Give the preparation type.
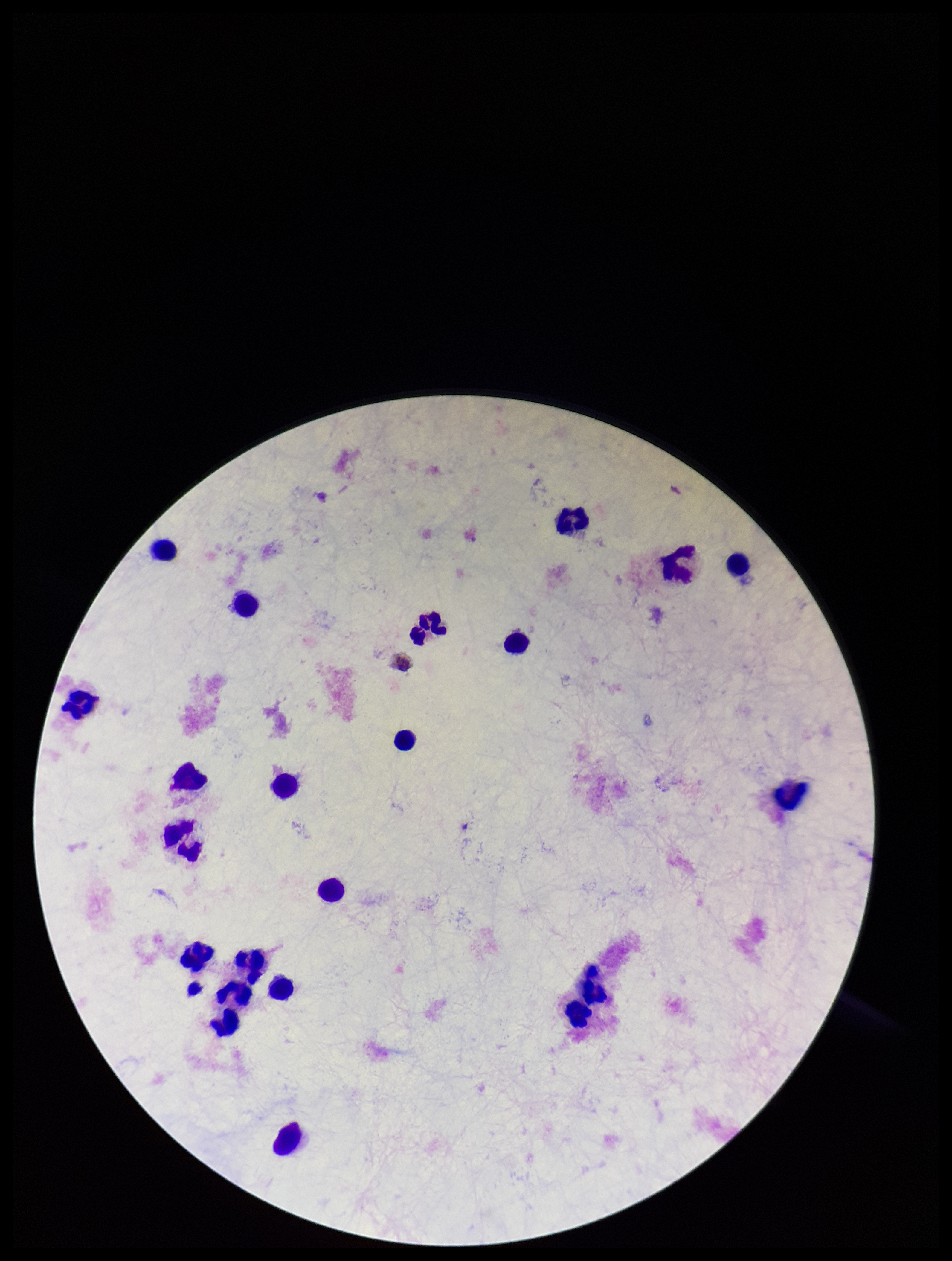
It is a thick blood smear.

Summary:
  - Leukocyte count: 23
  - Patient malaria status: negative
  - Field of view: one from this slide
  - Parasite count: 0
  - Image size: 952×1261 pixels
  - Stain: Giemsa
  - Capture: smartphone photograph through the microscope eyepiece
  - Plasmodium parasites: none detected